Assess for malaria.
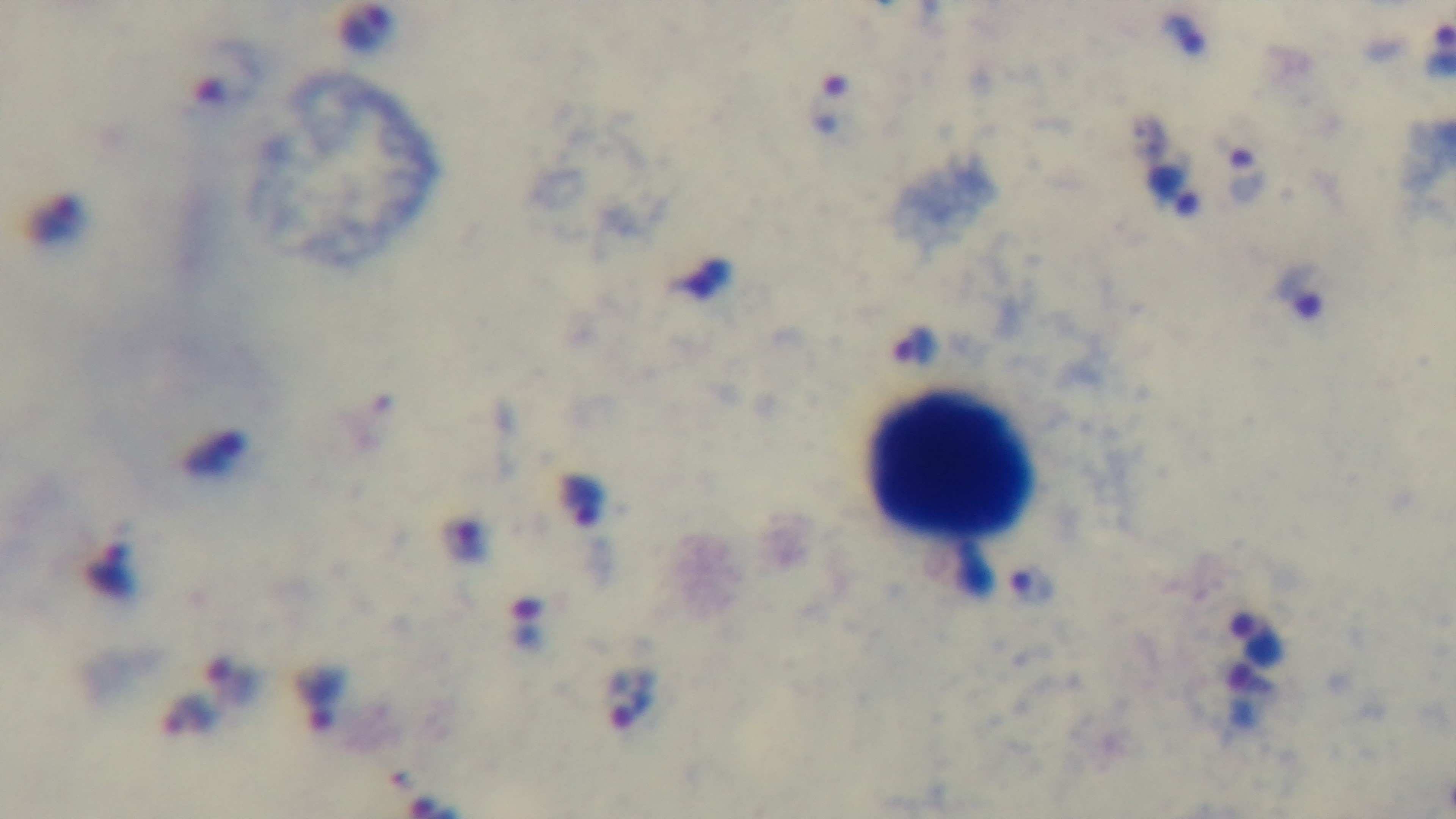
Infected.

Summary:
  - Objective: 100x oil immersion
  - Field of view: single
  - Modality: light microscopy
  - Preparation: thick
  - Stain: Giemsa
  - Capture: mounted 4K digital camera